Locate and identify every blood parasite.
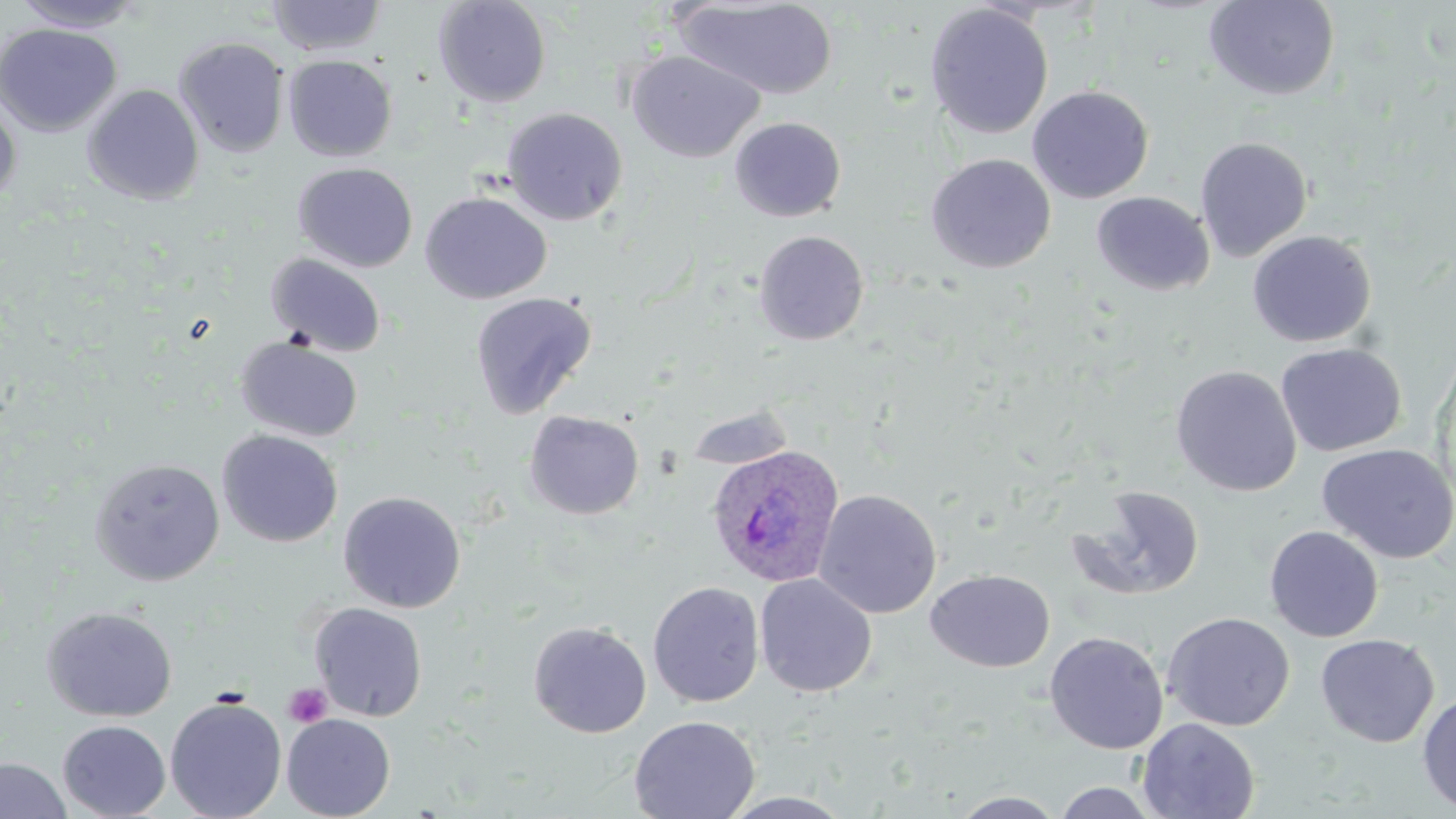

Approximate bounding boxes as [x1, y1, x2, y2] in pixels.
Plasmodium ovale-infected red blood cells: [706, 444, 846, 588].
No Plasmodium falciparum, Plasmodium malariae, Plasmodium vivax, Babesia divergens, or Trypanosoma brucei observed.

slide_level_diagnosis: Plasmodium ovale
stain: May-Grünwald-Giemsa
modality: light microscopy
image_size: 1456×819 pixels
field_of_view: one of a larger specimen
platelet_locations: 'approximate bounding boxes as [x1, y1, x2, y2] in pixels: [283, 683, 332, 728]'
magnification: 1000x
preparation: thin blood film
uninfected_red_blood_cell_locations: 'approximate bounding boxes as [x1, y1, x2, y2] in pixels: [10, 0, 145, 32], [265, 0, 387, 56], [433, 0, 551, 108], [1203, 0, 1341, 101], [675, 1, 838, 100], [924, 3, 1054, 140], [0, 23, 122, 137], [173, 37, 290, 158], [626, 50, 764, 163], [283, 55, 397, 161], [82, 84, 204, 206], [1027, 85, 1154, 204], [0, 98, 21, 207], [502, 107, 628, 226], [729, 117, 846, 221], [1194, 136, 1313, 262], [925, 153, 1056, 274], [293, 162, 418, 273], [420, 191, 552, 304], [1092, 191, 1214, 295], [753, 230, 870, 346], [1247, 230, 1377, 348], [265, 252, 387, 358], [469, 291, 598, 419], [235, 336, 363, 443], [1275, 342, 1408, 457], [1170, 365, 1303, 497], [683, 403, 798, 473], [524, 410, 644, 520], [217, 429, 343, 548], [1316, 443, 1456, 564], [89, 457, 225, 585], [1065, 485, 1205, 603], [814, 489, 941, 619], [338, 490, 466, 613], [1264, 525, 1384, 642], [925, 569, 1055, 672], [754, 573, 878, 698], [647, 581, 764, 707], [308, 602, 428, 721], [41, 606, 177, 722], [1162, 612, 1295, 732], [528, 620, 652, 738], [1044, 631, 1169, 754], [1315, 633, 1439, 747], [1417, 692, 1456, 814], [165, 697, 287, 819], [282, 713, 395, 819], [629, 715, 760, 819], [1136, 717, 1260, 819], [57, 720, 171, 819], [1, 757, 72, 819], [1049, 782, 1166, 818], [717, 791, 858, 818], [949, 791, 1069, 818]'